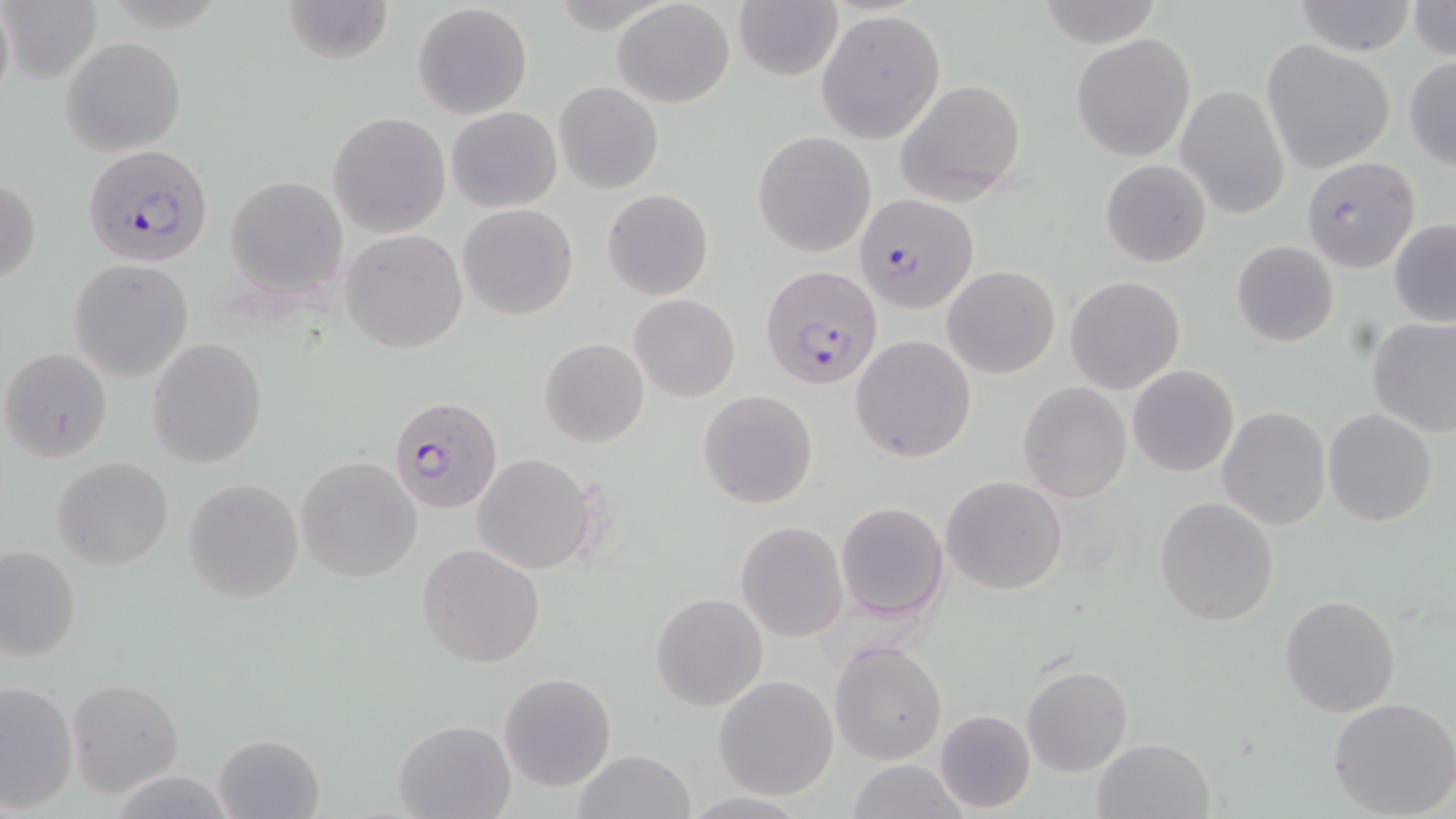
Summary:
  - Coordinate format: approximate bounding boxes as [x1, y1, x2, y2] in pixels
  - Plasmodium falciparum-infected red blood cell locations: [82, 144, 214, 266], [1300, 157, 1420, 273], [857, 193, 978, 315], [761, 265, 886, 392], [389, 396, 502, 514]
  - Uninfected red blood cell locations: [2, 0, 101, 82], [281, 0, 395, 66], [1035, 0, 1163, 49], [1290, 0, 1419, 56], [1407, 0, 1456, 61], [613, 1, 734, 107], [734, 2, 843, 81], [412, 3, 533, 118], [816, 10, 945, 143], [1071, 31, 1195, 162], [63, 36, 184, 156], [1261, 40, 1396, 175], [1405, 54, 1456, 171], [894, 79, 1027, 207], [554, 82, 664, 195], [1176, 85, 1290, 219], [447, 106, 562, 212], [328, 112, 451, 239], [753, 131, 876, 256], [1100, 159, 1212, 268], [224, 176, 348, 296], [0, 178, 41, 288], [602, 189, 714, 300], [458, 204, 578, 320], [1388, 219, 1456, 327], [341, 229, 468, 354], [1232, 240, 1340, 346], [69, 259, 195, 382], [943, 264, 1060, 379], [1065, 274, 1185, 394], [885, 276, 1021, 424], [630, 293, 740, 401], [1367, 318, 1456, 438], [851, 334, 977, 463], [146, 337, 268, 468], [539, 338, 649, 448], [1, 347, 114, 464], [1127, 364, 1240, 478], [1018, 382, 1132, 502], [698, 390, 818, 510], [1217, 406, 1331, 529], [1322, 409, 1438, 527], [472, 455, 599, 575], [296, 456, 422, 584], [52, 457, 174, 571], [941, 475, 1068, 595], [183, 479, 304, 603], [1154, 497, 1278, 626], [834, 500, 950, 620], [734, 520, 849, 642], [417, 544, 545, 666], [0, 545, 81, 662], [650, 592, 769, 712], [1279, 594, 1400, 718], [829, 640, 946, 765], [1021, 664, 1132, 777], [500, 672, 615, 791], [712, 675, 840, 800], [67, 678, 184, 798], [0, 679, 78, 813], [1328, 697, 1456, 819], [934, 708, 1036, 813], [393, 719, 514, 819], [213, 732, 324, 818], [1092, 737, 1214, 819], [573, 749, 694, 819], [848, 761, 970, 818]
  - Slide-level diagnosis: Plasmodium falciparum
  - Stain: May-Grünwald-Giemsa
  - Preparation: thin blood film
  - Modality: light microscopy
  - Magnification: 1000x
  - Field of view: single
  - Image size: 1456×819 pixels